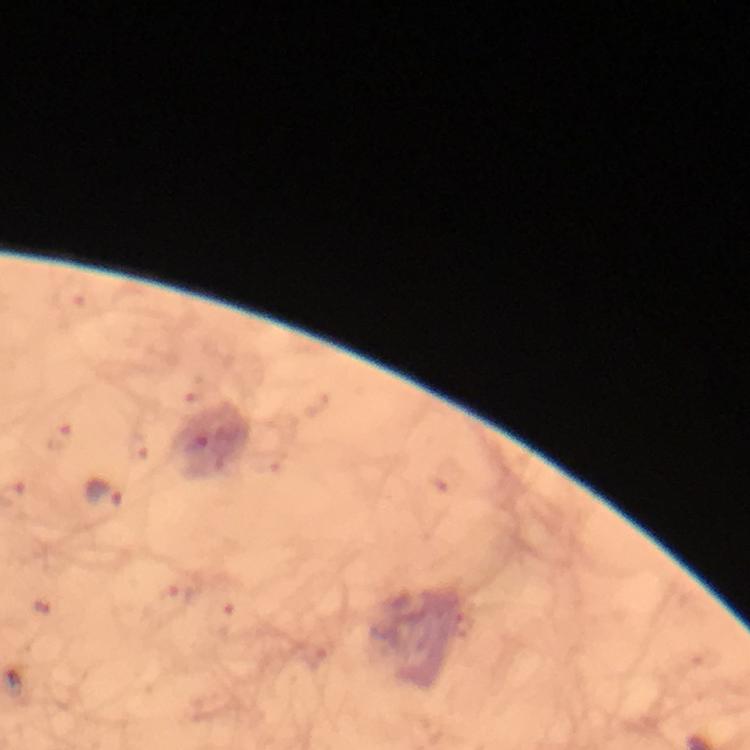

Approximate centers as {x, y} in pixels.
Summary:
  - Malaria parasite locations: {60, 438}, {102, 495}, {174, 599}, {464, 625}
  - Capture: smartphone photograph through a microscope
  - Context: from a malaria diagnostic workup
  - Preparation: thick blood film
  - Magnification: 100x
  - Cropped from: a single field of view
  - Stain: Giemsa
  - Image size: 750×750 pixels
  - Immersion oil: applied